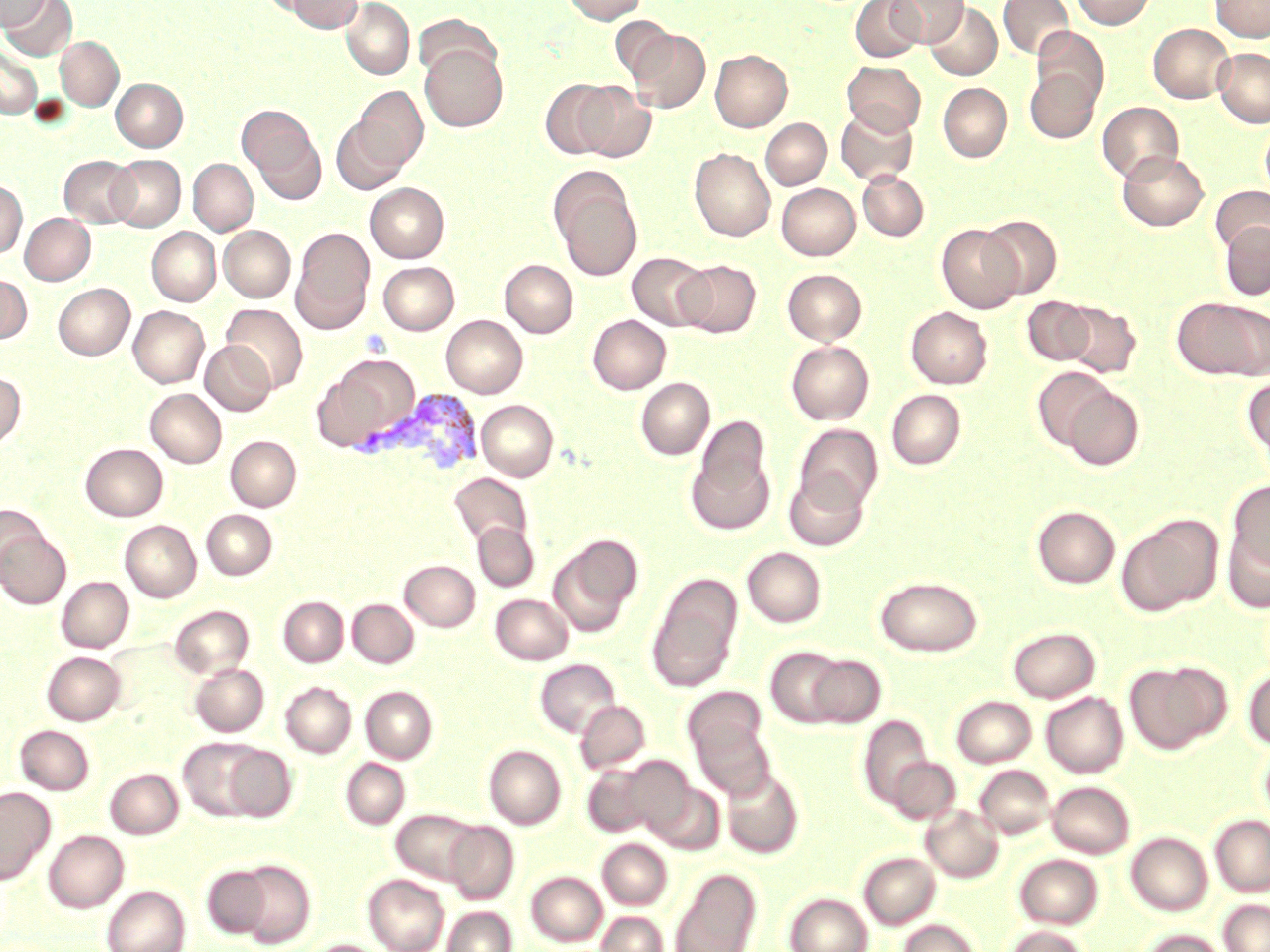
Approximate bounding boxes as named x1/y1/x2/y2 corners in pixels. Uninfected red blood cell locations: (x1=0, y1=0, x2=50, y2=31), (x1=1, y1=0, x2=77, y2=60), (x1=283, y1=0, x2=363, y2=33), (x1=341, y1=0, x2=415, y2=80), (x1=561, y1=0, x2=647, y2=24), (x1=850, y1=0, x2=925, y2=62), (x1=887, y1=0, x2=968, y2=47), (x1=998, y1=0, x2=1073, y2=59), (x1=1071, y1=0, x2=1156, y2=29), (x1=1210, y1=0, x2=1270, y2=42), (x1=925, y1=2, x2=1002, y2=80), (x1=413, y1=13, x2=501, y2=84), (x1=610, y1=16, x2=677, y2=82), (x1=1148, y1=23, x2=1234, y2=103), (x1=1033, y1=27, x2=1108, y2=107), (x1=628, y1=30, x2=711, y2=113), (x1=56, y1=37, x2=123, y2=110), (x1=420, y1=43, x2=508, y2=132), (x1=0, y1=45, x2=42, y2=119), (x1=1213, y1=48, x2=1270, y2=127), (x1=710, y1=50, x2=792, y2=132), (x1=843, y1=61, x2=925, y2=135), (x1=1025, y1=68, x2=1100, y2=143), (x1=111, y1=78, x2=187, y2=151), (x1=541, y1=79, x2=619, y2=159), (x1=574, y1=82, x2=656, y2=162), (x1=938, y1=83, x2=1012, y2=162), (x1=354, y1=86, x2=428, y2=169), (x1=1098, y1=102, x2=1184, y2=183), (x1=836, y1=105, x2=918, y2=185), (x1=239, y1=106, x2=318, y2=178), (x1=331, y1=117, x2=410, y2=195), (x1=761, y1=118, x2=831, y2=189), (x1=1260, y1=118, x2=1270, y2=202), (x1=251, y1=130, x2=326, y2=204), (x1=689, y1=148, x2=775, y2=241), (x1=1117, y1=151, x2=1209, y2=231), (x1=59, y1=155, x2=140, y2=227), (x1=107, y1=155, x2=185, y2=231), (x1=188, y1=159, x2=257, y2=235), (x1=550, y1=169, x2=642, y2=280), (x1=858, y1=171, x2=929, y2=241), (x1=0, y1=180, x2=27, y2=259), (x1=366, y1=183, x2=449, y2=262), (x1=777, y1=183, x2=860, y2=260), (x1=1210, y1=185, x2=1270, y2=256), (x1=20, y1=213, x2=95, y2=285), (x1=979, y1=215, x2=1062, y2=299), (x1=1219, y1=220, x2=1270, y2=300), (x1=936, y1=224, x2=1024, y2=313), (x1=219, y1=226, x2=295, y2=302), (x1=147, y1=227, x2=220, y2=305), (x1=292, y1=230, x2=373, y2=330), (x1=626, y1=252, x2=713, y2=330), (x1=500, y1=260, x2=578, y2=337), (x1=675, y1=260, x2=761, y2=338), (x1=379, y1=262, x2=459, y2=335), (x1=783, y1=269, x2=867, y2=345), (x1=0, y1=274, x2=31, y2=343), (x1=53, y1=283, x2=134, y2=360), (x1=1022, y1=296, x2=1097, y2=366), (x1=1173, y1=297, x2=1270, y2=381), (x1=1059, y1=301, x2=1141, y2=378), (x1=221, y1=304, x2=307, y2=394), (x1=128, y1=306, x2=209, y2=387), (x1=907, y1=306, x2=992, y2=388), (x1=441, y1=315, x2=527, y2=397), (x1=588, y1=315, x2=670, y2=394), (x1=200, y1=341, x2=276, y2=416), (x1=786, y1=341, x2=874, y2=424), (x1=321, y1=355, x2=419, y2=448), (x1=1031, y1=366, x2=1115, y2=450), (x1=0, y1=372, x2=26, y2=449), (x1=636, y1=377, x2=715, y2=459), (x1=1243, y1=377, x2=1270, y2=467), (x1=1060, y1=385, x2=1144, y2=471), (x1=146, y1=388, x2=226, y2=467), (x1=886, y1=389, x2=965, y2=469), (x1=477, y1=400, x2=558, y2=481), (x1=696, y1=415, x2=771, y2=498), (x1=794, y1=424, x2=883, y2=512), (x1=226, y1=436, x2=301, y2=511), (x1=81, y1=443, x2=168, y2=521), (x1=686, y1=450, x2=774, y2=534), (x1=784, y1=470, x2=869, y2=551), (x1=448, y1=472, x2=532, y2=547), (x1=1226, y1=481, x2=1270, y2=575), (x1=0, y1=503, x2=46, y2=581), (x1=1032, y1=506, x2=1120, y2=588), (x1=202, y1=510, x2=277, y2=579), (x1=1117, y1=514, x2=1223, y2=616), (x1=120, y1=520, x2=201, y2=601), (x1=472, y1=521, x2=538, y2=591), (x1=1223, y1=525, x2=1270, y2=613), (x1=0, y1=529, x2=71, y2=609), (x1=549, y1=536, x2=641, y2=637), (x1=742, y1=547, x2=826, y2=627), (x1=400, y1=560, x2=480, y2=631), (x1=646, y1=572, x2=744, y2=692), (x1=874, y1=576, x2=982, y2=656), (x1=57, y1=577, x2=133, y2=652), (x1=490, y1=593, x2=573, y2=664), (x1=278, y1=596, x2=348, y2=666), (x1=347, y1=599, x2=418, y2=668), (x1=169, y1=605, x2=254, y2=679), (x1=1008, y1=627, x2=1100, y2=702), (x1=765, y1=646, x2=851, y2=728), (x1=43, y1=651, x2=126, y2=725), (x1=805, y1=653, x2=886, y2=728), (x1=534, y1=658, x2=621, y2=738), (x1=1124, y1=661, x2=1228, y2=754), (x1=190, y1=663, x2=268, y2=736), (x1=1243, y1=667, x2=1270, y2=750), (x1=281, y1=682, x2=356, y2=757), (x1=361, y1=686, x2=437, y2=763), (x1=682, y1=686, x2=768, y2=766), (x1=1041, y1=691, x2=1128, y2=778), (x1=951, y1=695, x2=1036, y2=768), (x1=575, y1=700, x2=651, y2=774), (x1=858, y1=714, x2=934, y2=811), (x1=691, y1=721, x2=777, y2=800), (x1=15, y1=725, x2=94, y2=795), (x1=178, y1=738, x2=270, y2=821), (x1=222, y1=745, x2=297, y2=822), (x1=484, y1=745, x2=566, y2=829), (x1=886, y1=757, x2=960, y2=824), (x1=341, y1=758, x2=410, y2=830), (x1=594, y1=760, x2=669, y2=910), (x1=581, y1=761, x2=662, y2=838), (x1=975, y1=765, x2=1055, y2=839), (x1=721, y1=767, x2=804, y2=859), (x1=105, y1=769, x2=183, y2=838), (x1=645, y1=779, x2=725, y2=855), (x1=1047, y1=781, x2=1134, y2=858), (x1=0, y1=787, x2=55, y2=883), (x1=921, y1=805, x2=1003, y2=883), (x1=391, y1=809, x2=482, y2=885), (x1=1210, y1=815, x2=1270, y2=896), (x1=444, y1=821, x2=519, y2=904), (x1=44, y1=830, x2=128, y2=912), (x1=1125, y1=832, x2=1213, y2=916), (x1=597, y1=839, x2=672, y2=910), (x1=859, y1=852, x2=940, y2=929), (x1=1014, y1=854, x2=1103, y2=929), (x1=234, y1=861, x2=316, y2=947), (x1=202, y1=865, x2=273, y2=938), (x1=670, y1=867, x2=760, y2=952), (x1=526, y1=871, x2=607, y2=946), (x1=363, y1=874, x2=449, y2=952), (x1=102, y1=885, x2=189, y2=952), (x1=785, y1=892, x2=872, y2=952), (x1=1219, y1=899, x2=1270, y2=952), (x1=443, y1=906, x2=517, y2=952), (x1=596, y1=911, x2=668, y2=952), (x1=898, y1=919, x2=982, y2=952), (x1=1003, y1=925, x2=1091, y2=952), (x1=1139, y1=929, x2=1228, y2=952), (x1=307, y1=939, x2=387, y2=952). Platelet locations: (x1=359, y1=329, x2=393, y2=359). Plasmodium vivax-infected red blood cell locations: (x1=381, y1=389, x2=484, y2=476). Slide-level diagnosis: Plasmodium vivax. Single field of view. Image is 1270×952 pixels. Light microscopy. May-Grünwald-Giemsa stain. Captured at 1000x magnification. Thin blood smear.